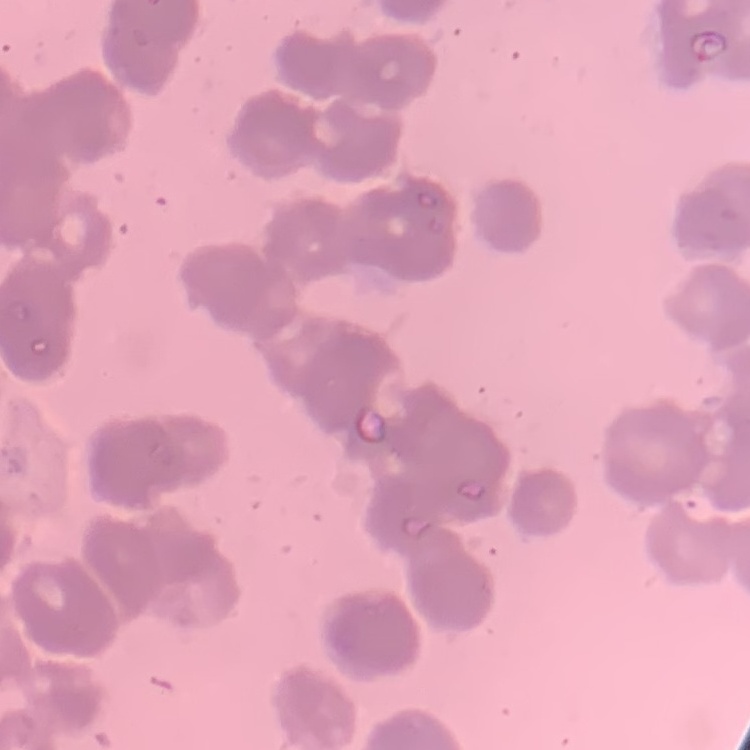
Summary:
  - Red blood cell morphology: rouleaux formation
  - Stain: Field's or Giemsa
  - Image type: square crop of a larger photomicrograph
  - Preparation: thin blood smear